Identify the parasite.
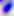
Toxoplasma gondii.

{
  "modality": "photomicrograph",
  "magnification": "400x"
}